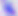

Micrograph. Toxoplasma gondii is shown. 400x magnification.